Assess the morphology of the erythrocytes.
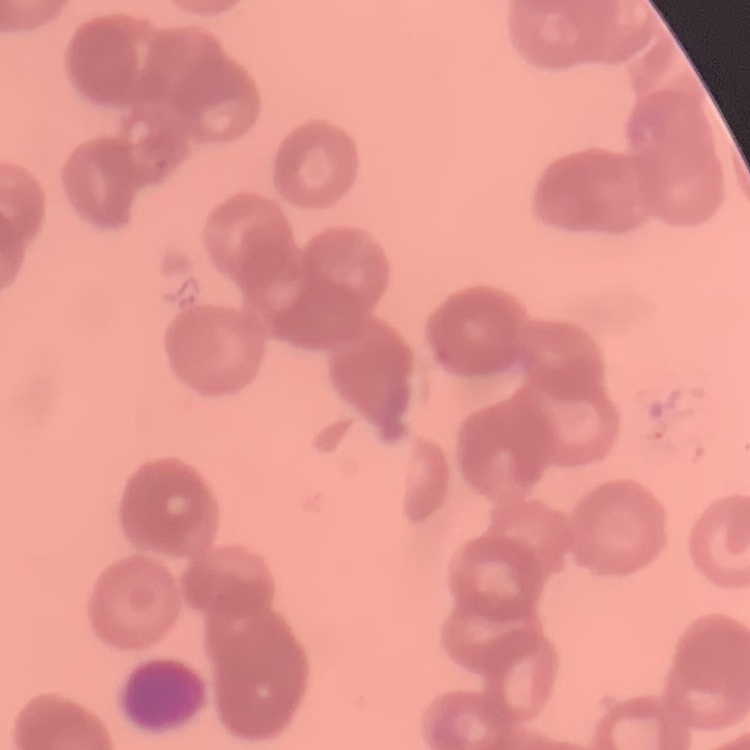
They show rouleaux formation.

stain: Field's or Giemsa
image_type: square crop of a larger photomicrograph
preparation: thin blood film